Report the malaria status of this cell.
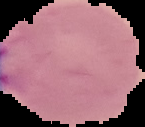

Parasitized.

From a thin blood smear. Image is 145×127 pixels. Segmented cell region on a black background.